Outline each uninfected red blood cell.
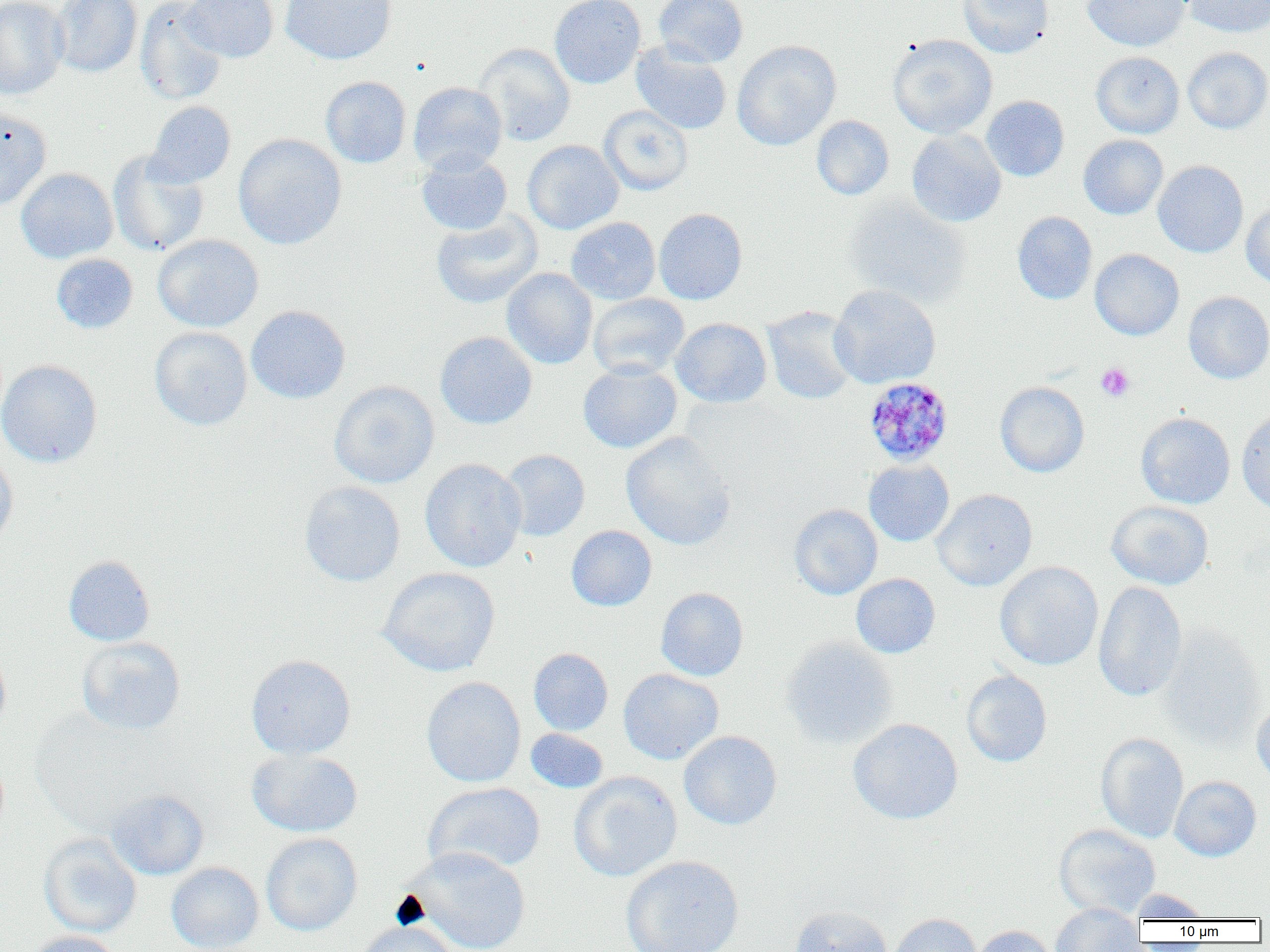

Approximate bounding boxes as [x1, y1, x2, y2] in pixels.
Uninfected red blood cells: [0, 0, 69, 99], [50, 0, 142, 78], [135, 0, 228, 105], [181, 0, 279, 63], [280, 0, 396, 64], [549, 0, 646, 89], [654, 0, 748, 68], [958, 0, 1052, 57], [1082, 0, 1190, 51], [1183, 0, 1270, 38], [887, 34, 997, 138], [732, 40, 841, 150], [631, 41, 732, 135], [473, 43, 576, 146], [1182, 47, 1270, 133], [1090, 51, 1184, 139], [320, 76, 411, 168], [408, 81, 507, 175], [981, 95, 1069, 181], [146, 101, 236, 188], [599, 106, 693, 195], [0, 108, 51, 211], [811, 116, 894, 200], [906, 129, 1006, 227], [233, 133, 347, 249], [1078, 134, 1168, 220], [522, 140, 623, 234], [108, 151, 208, 256], [416, 152, 513, 235], [1153, 160, 1248, 258], [16, 168, 118, 263], [843, 195, 972, 307], [1241, 202, 1270, 288], [654, 208, 748, 305], [1012, 211, 1097, 304], [431, 212, 543, 309], [566, 217, 660, 304], [152, 234, 264, 332], [1090, 249, 1184, 340], [51, 253, 138, 334], [501, 268, 598, 369], [829, 284, 941, 389], [1183, 291, 1270, 384], [588, 293, 690, 380], [246, 305, 350, 404], [761, 306, 861, 405], [671, 318, 772, 408], [150, 327, 253, 431], [435, 331, 537, 429], [0, 359, 102, 468], [578, 362, 682, 453], [328, 380, 440, 489], [995, 382, 1089, 477], [1236, 409, 1270, 514], [1135, 412, 1235, 508], [621, 432, 737, 551], [499, 449, 590, 541], [0, 451, 18, 552], [420, 458, 527, 572], [863, 459, 954, 546], [299, 481, 406, 586], [932, 489, 1037, 591], [1106, 500, 1213, 590], [789, 504, 883, 600], [566, 525, 657, 611], [63, 555, 155, 646], [994, 561, 1103, 670], [378, 567, 500, 677], [851, 573, 940, 658], [1093, 581, 1187, 702], [655, 587, 748, 681], [1157, 625, 1266, 748], [76, 636, 186, 735], [780, 636, 898, 749], [0, 645, 11, 736], [528, 648, 613, 736], [246, 654, 356, 759], [618, 668, 723, 764], [961, 670, 1052, 767], [421, 676, 526, 787], [1251, 701, 1270, 790], [848, 718, 963, 824], [525, 728, 609, 793], [678, 730, 782, 830], [1095, 732, 1189, 843], [246, 747, 362, 837], [568, 771, 682, 882], [1170, 776, 1261, 861], [423, 782, 546, 876], [106, 788, 209, 880], [1054, 823, 1161, 918], [261, 833, 362, 936], [38, 834, 142, 937], [404, 847, 532, 952], [621, 855, 744, 952], [166, 862, 263, 952], [1129, 889, 1212, 921], [1050, 903, 1146, 952], [789, 905, 892, 952], [888, 913, 981, 952], [353, 920, 459, 952], [970, 925, 1058, 952], [25, 931, 123, 952].

Plasmodium malariae-infected red blood cell locations: [863, 377, 954, 466]. Platelet locations: [1096, 363, 1135, 401]. Slide-level diagnosis: Plasmodium malariae. Optical microscopy. Thin blood film. One field of a larger specimen. Image is 1270×952 pixels. Captured at 1000x magnification.